Identify the parasite.
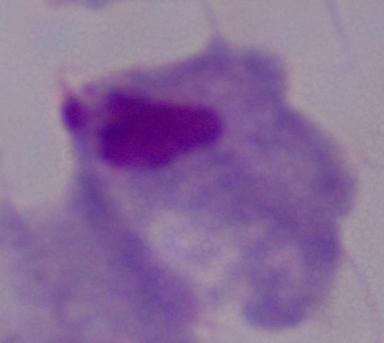

A trichomonad.

Summary:
  - Magnification: 1000x
  - Modality: micrograph